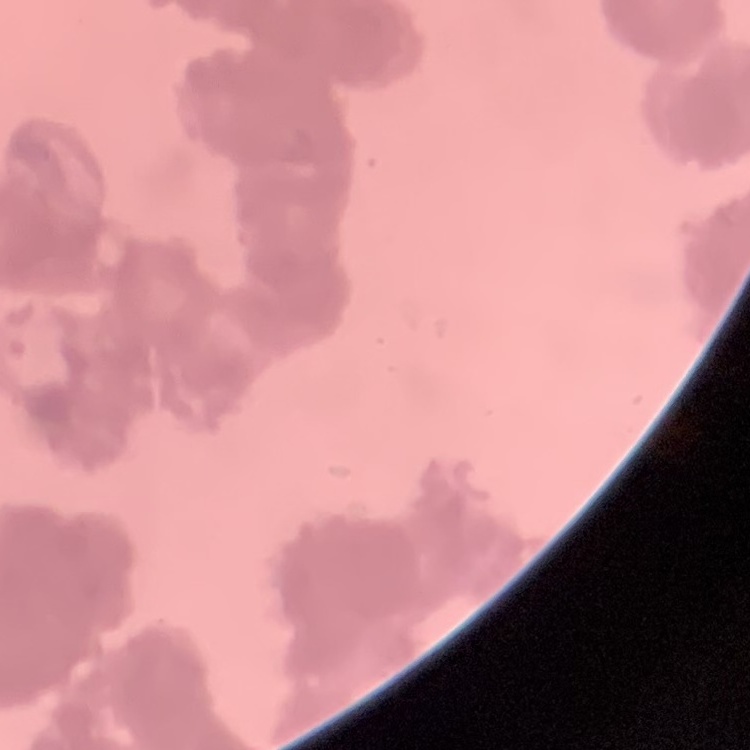
The erythrocytes show rouleaux formation. Stained with either Field's or Giemsa. Thin blood smear. Square crop of a larger photomicrograph.